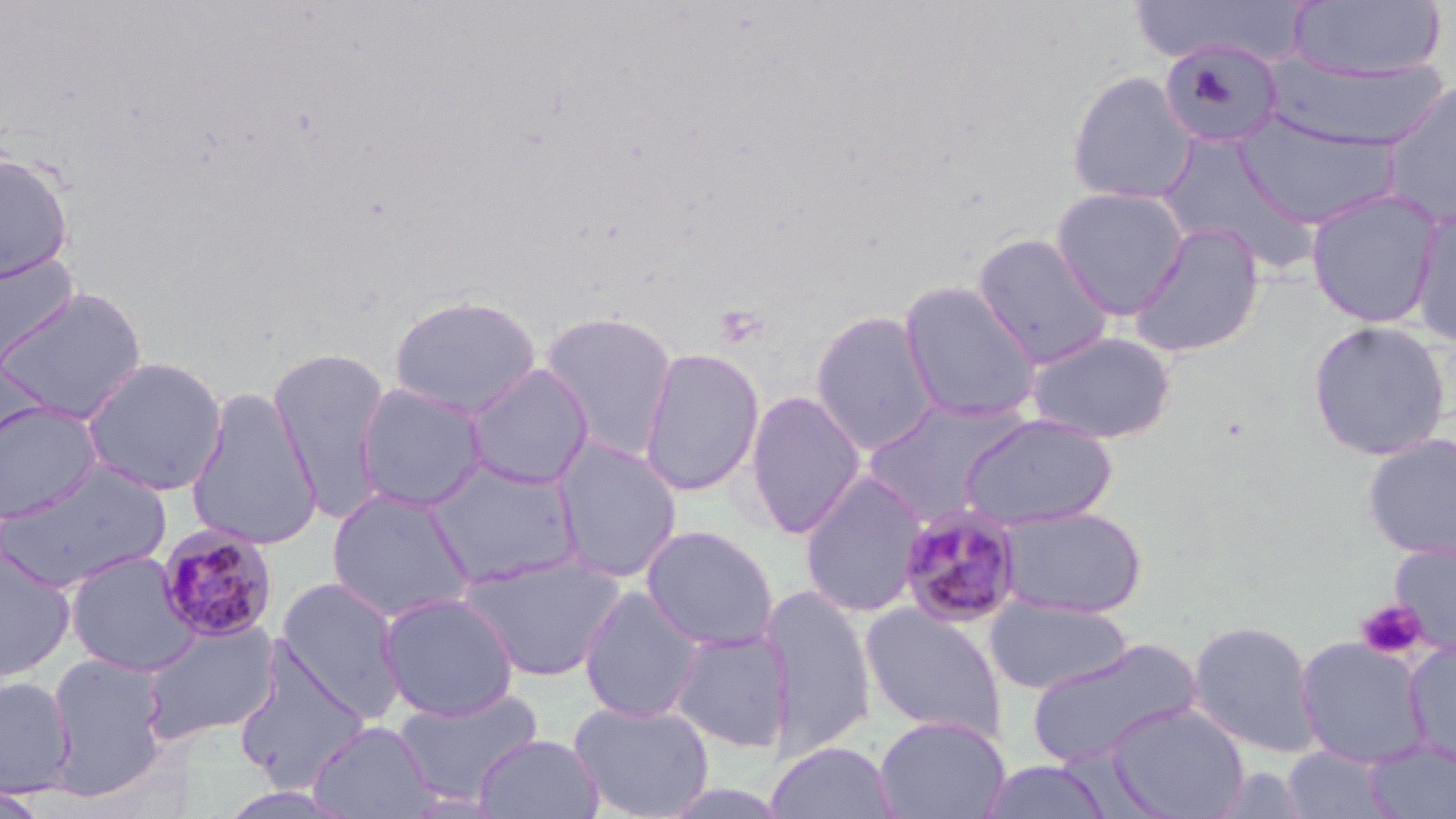
Summary:
  - Coordinate format: approximate bounding boxes as named x1/y1/x2/y2 corners in pixels
  - Plasmodium malariae-infected red blood cell locations: (x1=898, y1=503, x2=1025, y2=628), (x1=154, y1=523, x2=281, y2=643)
  - Uninfected red blood cell locations: (x1=1127, y1=0, x2=1311, y2=67), (x1=1289, y1=1, x2=1448, y2=83), (x1=1158, y1=40, x2=1284, y2=152), (x1=1265, y1=54, x2=1449, y2=150), (x1=1065, y1=70, x2=1197, y2=206), (x1=1377, y1=80, x2=1456, y2=226), (x1=1232, y1=110, x2=1401, y2=230), (x1=1158, y1=132, x2=1318, y2=271), (x1=0, y1=151, x2=75, y2=285), (x1=1050, y1=185, x2=1191, y2=320), (x1=1305, y1=188, x2=1444, y2=329), (x1=1409, y1=206, x2=1456, y2=346), (x1=1128, y1=222, x2=1265, y2=358), (x1=971, y1=233, x2=1114, y2=369), (x1=1, y1=251, x2=80, y2=371), (x1=897, y1=279, x2=1043, y2=423), (x1=0, y1=285, x2=148, y2=424), (x1=388, y1=294, x2=542, y2=417), (x1=537, y1=309, x2=680, y2=461), (x1=809, y1=309, x2=941, y2=456), (x1=1306, y1=319, x2=1451, y2=461), (x1=1024, y1=329, x2=1178, y2=444), (x1=267, y1=345, x2=394, y2=522), (x1=638, y1=346, x2=765, y2=497), (x1=80, y1=355, x2=229, y2=496), (x1=464, y1=363, x2=594, y2=491), (x1=353, y1=381, x2=490, y2=512), (x1=185, y1=387, x2=324, y2=550), (x1=743, y1=390, x2=866, y2=539), (x1=860, y1=397, x2=1033, y2=526), (x1=0, y1=401, x2=104, y2=523), (x1=959, y1=413, x2=1119, y2=532), (x1=1361, y1=431, x2=1456, y2=561), (x1=551, y1=436, x2=684, y2=583), (x1=422, y1=457, x2=584, y2=590), (x1=0, y1=460, x2=173, y2=594), (x1=798, y1=470, x2=928, y2=619), (x1=325, y1=487, x2=475, y2=624), (x1=993, y1=504, x2=1148, y2=618), (x1=640, y1=524, x2=780, y2=651), (x1=1387, y1=540, x2=1456, y2=655), (x1=0, y1=545, x2=77, y2=684), (x1=64, y1=550, x2=201, y2=677), (x1=455, y1=551, x2=626, y2=683), (x1=274, y1=577, x2=408, y2=722), (x1=578, y1=585, x2=705, y2=723), (x1=759, y1=585, x2=878, y2=759), (x1=378, y1=591, x2=520, y2=722), (x1=985, y1=596, x2=1134, y2=695), (x1=859, y1=602, x2=1009, y2=742), (x1=140, y1=617, x2=280, y2=746), (x1=1187, y1=619, x2=1322, y2=758), (x1=667, y1=629, x2=795, y2=753), (x1=1294, y1=635, x2=1431, y2=767), (x1=1024, y1=636, x2=1203, y2=770), (x1=1403, y1=640, x2=1456, y2=766), (x1=232, y1=643, x2=372, y2=793), (x1=44, y1=652, x2=171, y2=799), (x1=0, y1=675, x2=76, y2=798), (x1=392, y1=688, x2=544, y2=805), (x1=569, y1=699, x2=715, y2=819), (x1=1107, y1=702, x2=1250, y2=819), (x1=873, y1=715, x2=1011, y2=819), (x1=308, y1=720, x2=438, y2=819), (x1=473, y1=732, x2=604, y2=818), (x1=1363, y1=738, x2=1456, y2=818), (x1=764, y1=740, x2=900, y2=819), (x1=1280, y1=746, x2=1395, y2=818), (x1=973, y1=758, x2=1118, y2=818), (x1=0, y1=782, x2=53, y2=818)
  - Platelet locations: (x1=1356, y1=599, x2=1429, y2=662)
  - Slide-level diagnosis: Plasmodium malariae
  - Image size: 1456×819 pixels
  - Magnification: 1000x
  - Modality: optical microscopy
  - Field of view: one of a larger specimen
  - Preparation: thin blood film
  - Stain: May-Grünwald-Giemsa